Outline each uninfected red blood cell.
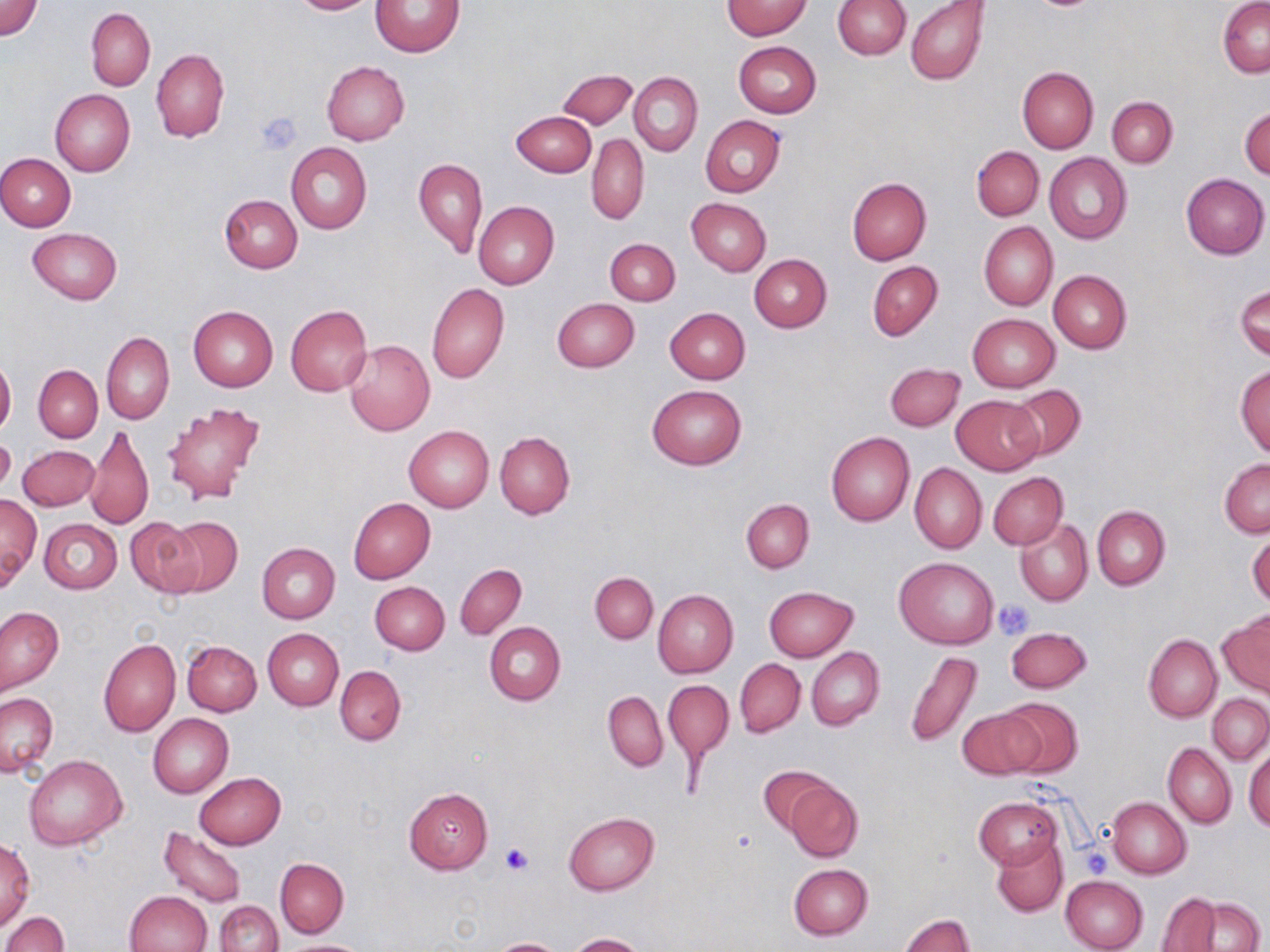
Approximate bounding boxes as (x1,y1)-(x2,y2) corner pairs in pixels.
Uninfected red blood cells: (289,0)-(381,15), (371,0)-(465,58), (2,1)-(42,41), (722,1)-(812,39), (832,1)-(909,59), (905,1)-(989,86), (1218,1)-(1269,77), (86,7)-(155,91), (733,41)-(822,117), (150,49)-(229,141), (321,60)-(410,145), (1017,66)-(1098,154), (558,69)-(637,130), (629,72)-(702,156), (50,88)-(135,176), (1107,96)-(1177,167), (1240,106)-(1269,181), (512,110)-(596,176), (700,116)-(786,197), (587,133)-(649,224), (286,143)-(372,233), (971,146)-(1044,221), (1045,152)-(1132,244), (1,154)-(76,232), (414,158)-(487,259), (1181,174)-(1269,259), (846,178)-(933,264), (219,194)-(303,273), (686,197)-(771,276), (473,201)-(559,289), (978,222)-(1058,310), (28,228)-(121,304), (605,238)-(679,306), (750,254)-(831,332), (867,260)-(943,341), (1048,270)-(1132,353), (427,283)-(509,384), (1236,285)-(1269,361), (552,297)-(639,373), (285,305)-(372,397), (188,306)-(278,391), (665,307)-(750,383), (968,314)-(1060,392), (101,332)-(174,424), (344,338)-(435,436), (0,354)-(16,438), (885,363)-(965,431), (1236,364)-(1270,458), (33,365)-(103,442), (648,384)-(746,470), (1006,384)-(1086,462), (952,395)-(1043,474), (162,401)-(264,504), (85,422)-(154,531), (404,426)-(493,512), (495,431)-(575,518), (826,431)-(915,526), (0,432)-(15,497), (18,445)-(99,511), (1220,458)-(1270,538), (909,463)-(987,555), (988,472)-(1067,549), (0,493)-(41,591), (349,497)-(435,583), (741,499)-(814,572), (1092,506)-(1170,589), (164,516)-(243,598), (1016,517)-(1093,606), (40,518)-(123,594), (126,518)-(203,598), (1248,529)-(1269,609), (256,543)-(339,623), (895,557)-(999,648), (455,564)-(527,639), (590,572)-(658,643), (370,581)-(449,655), (764,586)-(859,662), (653,589)-(738,677), (1,606)-(63,695), (1219,612)-(1270,699), (484,621)-(567,705), (1005,627)-(1092,694), (263,629)-(344,709), (1144,633)-(1222,722), (97,638)-(180,736), (182,640)-(262,716), (807,648)-(884,730), (905,650)-(983,749), (735,658)-(806,737), (335,665)-(406,745), (664,680)-(733,764), (603,691)-(667,771), (1,693)-(58,777), (1207,693)-(1269,764), (999,696)-(1083,777), (958,706)-(1045,780), (148,714)-(234,798), (1164,742)-(1235,827), (1245,743)-(1270,832), (24,754)-(126,849), (758,765)-(836,834), (194,772)-(286,849), (784,779)-(864,862), (403,788)-(493,873), (975,797)-(1063,869), (1107,797)-(1191,878), (564,812)-(659,895), (157,826)-(247,908), (1,837)-(34,933), (992,837)-(1068,916), (275,858)-(348,937), (788,863)-(872,939), (1060,875)-(1149,952), (125,891)-(212,952), (1157,892)-(1224,951), (1189,897)-(1263,951), (216,900)-(282,952), (2,911)-(69,952), (900,914)-(975,952), (567,933)-(647,952), (488,938)-(569,952), (281,939)-(366,951).

Platelet locations: (255,111)-(303,151), (993,599)-(1036,639), (501,843)-(533,875), (1080,846)-(1113,876). Slide-level diagnosis: negative for blood parasites. Optical microscopy. May-Grünwald-Giemsa-stained preparation. One field of a larger specimen. Image is 1270×952 pixels. Thin blood film. Captured at 1000x magnification.